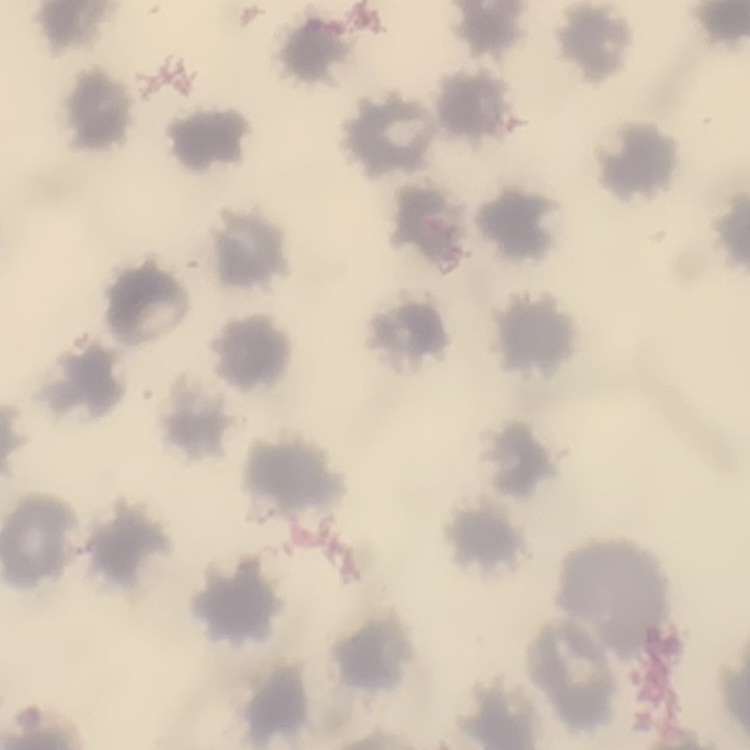 The red blood cells exhibit no rouleaux formation. One tile cut from a larger photomicrograph. Thin peripheral smear. Stained with either Field's or Giemsa.